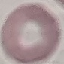

Result: negative for malaria parasites. Automatically extracted cell patch, resized to 64 × 64 pixels. Thin smear of blood. Giemsa stain. Photographed with a smartphone camera at the microscope eyepiece.